Look for parasitized red blood cells.
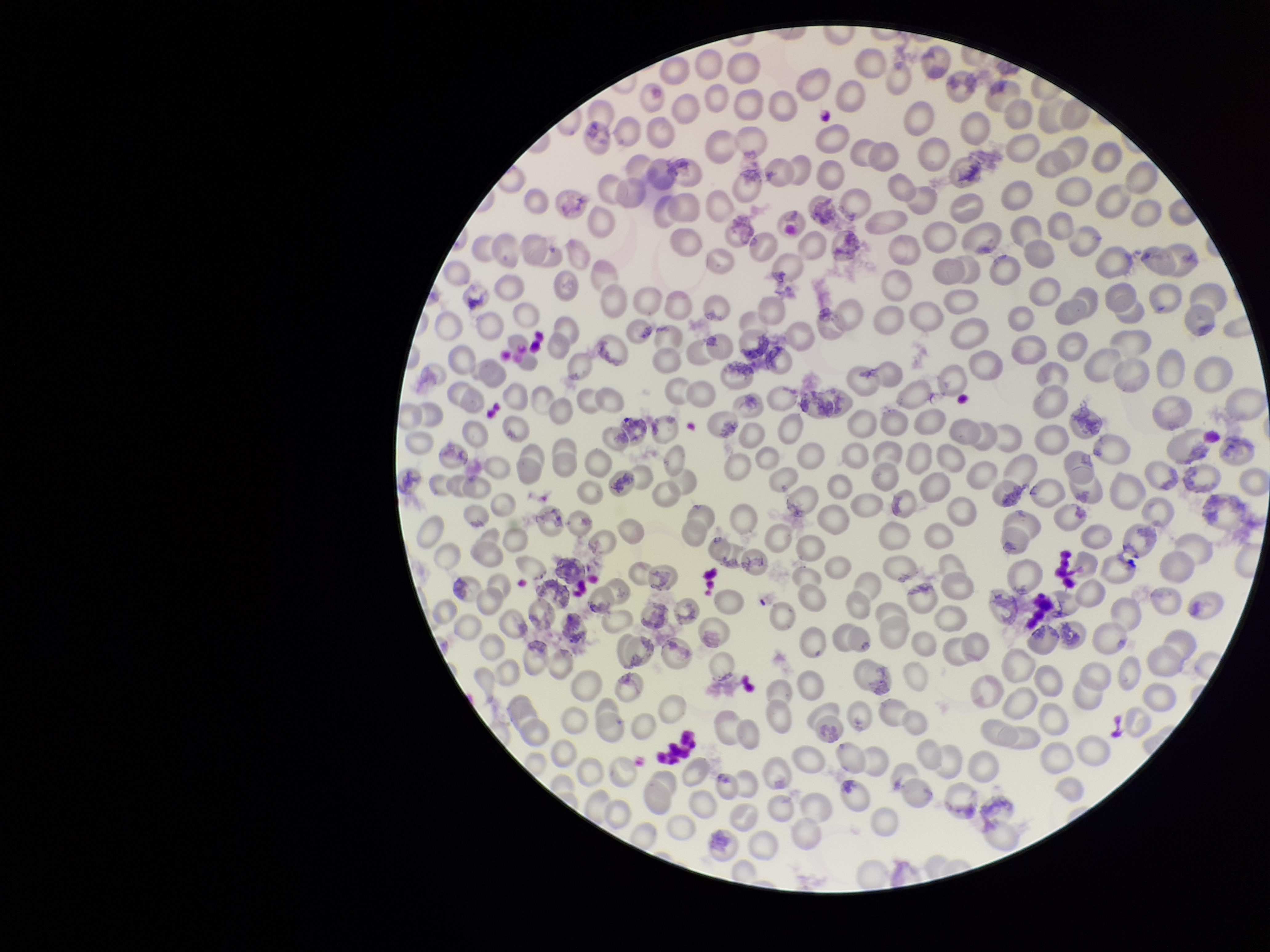

None identified.

capture = smartphone photograph through the microscope eyepiece
patient malaria status = negative
field of view = one from this slide
preparation = thin smear
red blood cell count = 230
stain = Giemsa
image size = 1270×952 pixels
parasitized red blood cell count = 0